Comment on the morphology of the red blood cells.
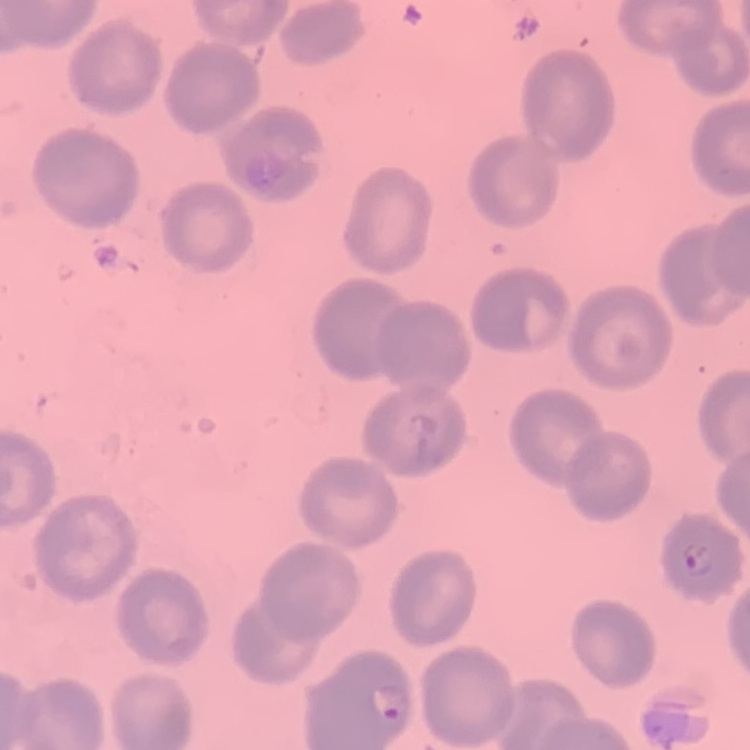
No rouleaux formation.

{
  "preparation": "thin blood smear",
  "stain": "Field's or Giemsa",
  "image_type": "one tile cut from a larger photomicrograph"
}